Locate every malaria parasite.
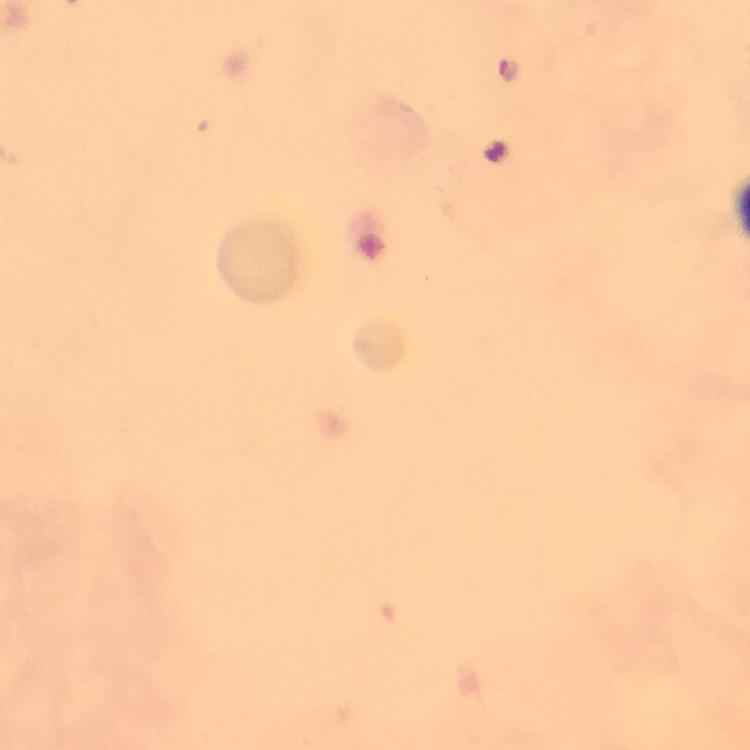

Approximate centers as [x, y] in pixels.
Malaria parasites: [504, 70].

A crop from one field of view. Thick blood smear. Giemsa stain. Immersion oil applied. Smartphone photograph taken through a microscope. Image is 750×750 pixels. 100x magnification. From a diagnostic examination for malaria.